Identify the parasite.
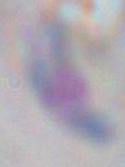

This is Toxoplasma gondii.

Summary:
  - Magnification: 1000x
  - Modality: micrograph